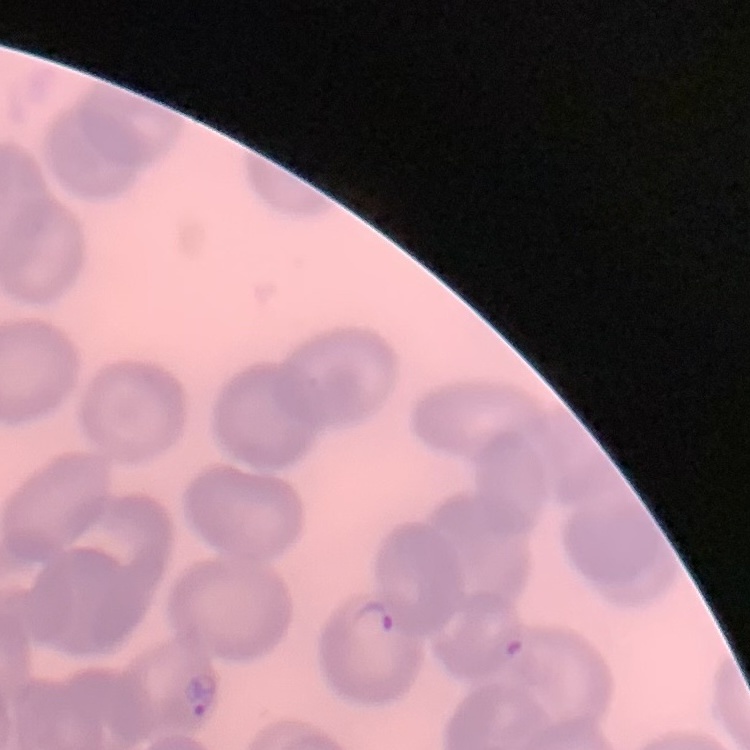
erythrocyte morphology = no rouleaux formation
stain = Field's or Giemsa
preparation = thin peripheral smear
image type = square crop of a larger photomicrograph